Give the extent of all uninfected red blood cells.
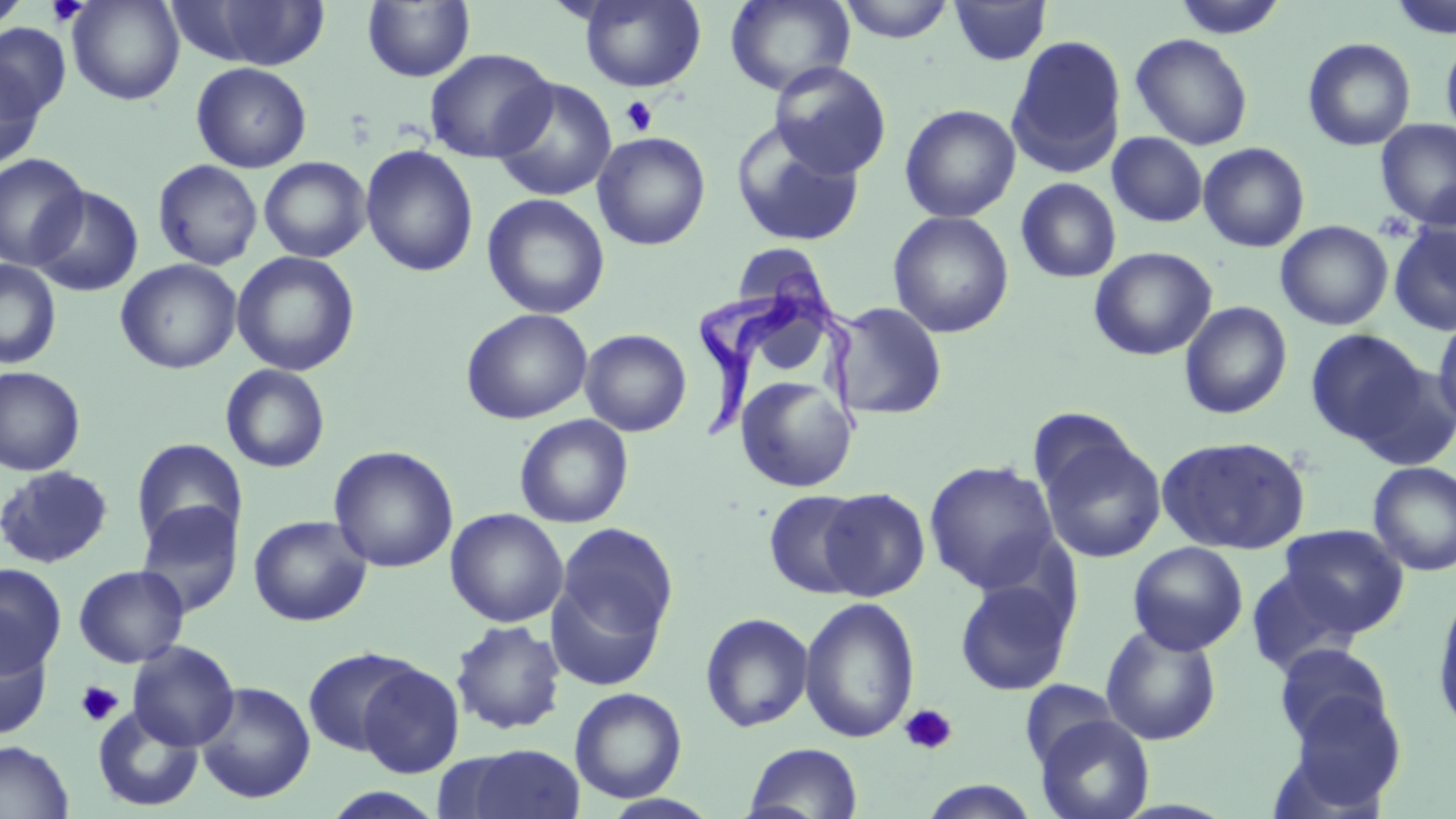

Approximate bounding boxes as named x1/y1/x2/y2 corners in pixels.
Uninfected red blood cells: (x1=0, y1=0, x2=31, y2=31), (x1=66, y1=0, x2=184, y2=105), (x1=171, y1=0, x2=334, y2=70), (x1=579, y1=0, x2=706, y2=92), (x1=725, y1=0, x2=855, y2=96), (x1=836, y1=0, x2=957, y2=43), (x1=1173, y1=0, x2=1288, y2=39), (x1=1388, y1=0, x2=1456, y2=40), (x1=362, y1=1, x2=475, y2=82), (x1=948, y1=1, x2=1051, y2=66), (x1=0, y1=24, x2=70, y2=121), (x1=1440, y1=32, x2=1456, y2=146), (x1=1130, y1=33, x2=1253, y2=151), (x1=1007, y1=34, x2=1127, y2=175), (x1=1302, y1=37, x2=1416, y2=152), (x1=424, y1=48, x2=557, y2=163), (x1=0, y1=57, x2=46, y2=170), (x1=769, y1=61, x2=892, y2=180), (x1=191, y1=62, x2=312, y2=173), (x1=491, y1=77, x2=617, y2=202), (x1=899, y1=104, x2=1021, y2=222), (x1=1375, y1=119, x2=1456, y2=229), (x1=731, y1=122, x2=866, y2=248), (x1=592, y1=132, x2=711, y2=250), (x1=1107, y1=132, x2=1208, y2=227), (x1=1198, y1=142, x2=1310, y2=252), (x1=360, y1=144, x2=479, y2=277), (x1=0, y1=153, x2=90, y2=271), (x1=259, y1=157, x2=371, y2=262), (x1=152, y1=160, x2=263, y2=271), (x1=1015, y1=177, x2=1122, y2=283), (x1=30, y1=186, x2=144, y2=297), (x1=482, y1=193, x2=611, y2=319), (x1=888, y1=211, x2=1014, y2=338), (x1=1276, y1=220, x2=1393, y2=330), (x1=1388, y1=221, x2=1456, y2=336), (x1=731, y1=243, x2=830, y2=316), (x1=1089, y1=247, x2=1217, y2=361), (x1=231, y1=251, x2=360, y2=376), (x1=116, y1=259, x2=242, y2=374), (x1=0, y1=260, x2=61, y2=369), (x1=829, y1=301, x2=948, y2=421), (x1=1179, y1=301, x2=1293, y2=419), (x1=460, y1=308, x2=593, y2=425), (x1=1432, y1=314, x2=1456, y2=432), (x1=579, y1=328, x2=691, y2=437), (x1=1305, y1=328, x2=1429, y2=449), (x1=220, y1=364, x2=331, y2=473), (x1=0, y1=366, x2=86, y2=476), (x1=735, y1=376, x2=857, y2=492), (x1=515, y1=414, x2=634, y2=527), (x1=1035, y1=426, x2=1167, y2=565), (x1=1156, y1=435, x2=1311, y2=555), (x1=131, y1=438, x2=246, y2=549), (x1=328, y1=445, x2=458, y2=573), (x1=924, y1=460, x2=1061, y2=594), (x1=1368, y1=461, x2=1456, y2=576), (x1=0, y1=464, x2=114, y2=568), (x1=819, y1=487, x2=930, y2=601), (x1=763, y1=489, x2=872, y2=599), (x1=134, y1=501, x2=243, y2=618), (x1=445, y1=508, x2=568, y2=627), (x1=248, y1=514, x2=372, y2=627), (x1=552, y1=521, x2=678, y2=663), (x1=1278, y1=523, x2=1409, y2=634), (x1=1127, y1=542, x2=1248, y2=656), (x1=0, y1=563, x2=67, y2=676), (x1=73, y1=564, x2=190, y2=668), (x1=1245, y1=566, x2=1366, y2=678), (x1=954, y1=577, x2=1074, y2=696), (x1=1431, y1=593, x2=1456, y2=733), (x1=799, y1=596, x2=920, y2=744), (x1=700, y1=612, x2=814, y2=733), (x1=450, y1=620, x2=566, y2=735), (x1=1100, y1=623, x2=1222, y2=745), (x1=0, y1=632, x2=53, y2=740), (x1=127, y1=640, x2=240, y2=751), (x1=1273, y1=644, x2=1395, y2=752), (x1=302, y1=647, x2=424, y2=758), (x1=356, y1=662, x2=464, y2=778), (x1=1020, y1=679, x2=1121, y2=771), (x1=195, y1=681, x2=316, y2=804), (x1=570, y1=687, x2=687, y2=803), (x1=1281, y1=688, x2=1407, y2=810), (x1=92, y1=705, x2=203, y2=812), (x1=1034, y1=714, x2=1155, y2=819), (x1=0, y1=739, x2=74, y2=819), (x1=743, y1=742, x2=864, y2=819), (x1=458, y1=744, x2=585, y2=819), (x1=915, y1=780, x2=1044, y2=818), (x1=319, y1=787, x2=448, y2=819), (x1=599, y1=794, x2=721, y2=819).

Platelet locations: (x1=46, y1=0, x2=90, y2=25), (x1=620, y1=96, x2=658, y2=136), (x1=1372, y1=211, x2=1417, y2=244), (x1=75, y1=680, x2=123, y2=727), (x1=899, y1=703, x2=957, y2=756). Trypanosoma brucei locations: (x1=695, y1=269, x2=882, y2=445). Slide-level diagnosis: Trypanosoma brucei. Single field of view. Captured at 1000x magnification. Thin blood smear. May-Grünwald-Giemsa-stained preparation. Light microscopy. Image is 1456×819 pixels.